Comment on the morphology of the red blood cells.
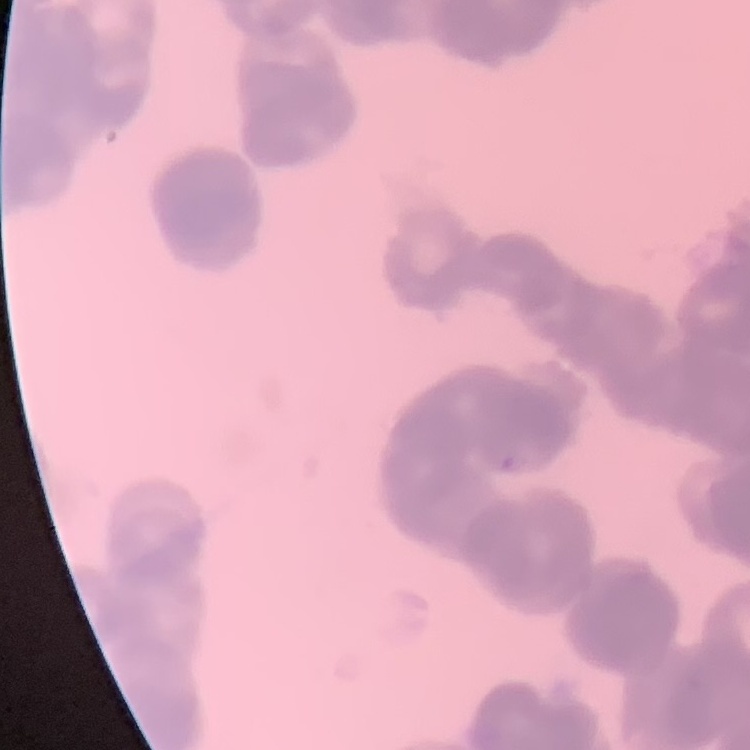
They show rouleaux formation.

preparation = thin blood film
stain = Field's or Giemsa
image type = square crop of a larger photomicrograph